Give the extent of all white blood cells.
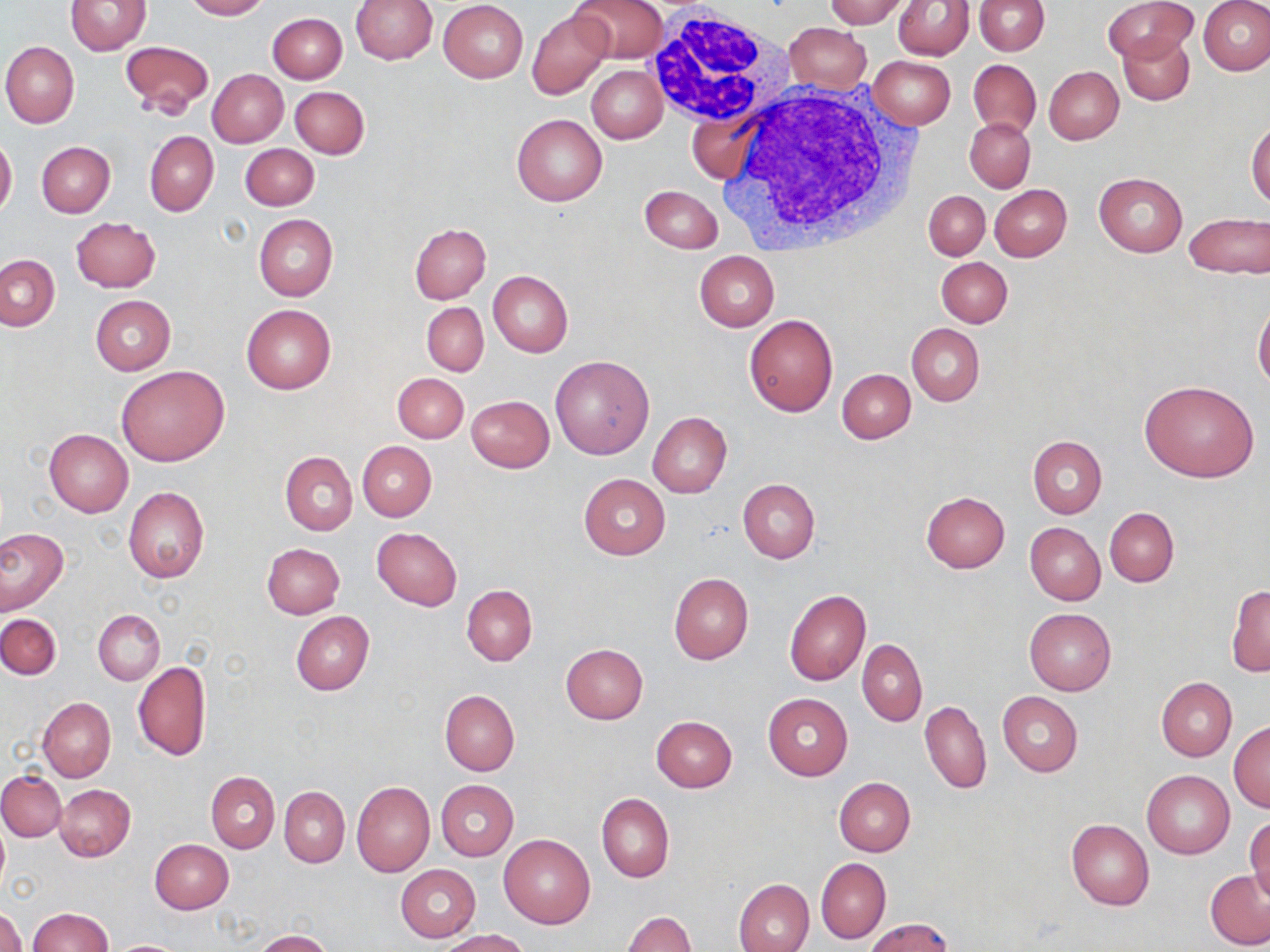

Approximate bounding boxes as named x1/y1/x2/y2 corners in pixels.
White blood cells: (x1=643, y1=9, x2=794, y2=129), (x1=716, y1=78, x2=918, y2=252).

Uninfected red blood cell locations: (x1=183, y1=0, x2=268, y2=20), (x1=350, y1=0, x2=438, y2=64), (x1=571, y1=0, x2=667, y2=63), (x1=824, y1=0, x2=909, y2=27), (x1=895, y1=0, x2=973, y2=59), (x1=1105, y1=0, x2=1193, y2=62), (x1=65, y1=1, x2=150, y2=56), (x1=439, y1=1, x2=528, y2=82), (x1=975, y1=1, x2=1049, y2=55), (x1=1198, y1=1, x2=1270, y2=76), (x1=527, y1=9, x2=613, y2=99), (x1=267, y1=12, x2=347, y2=83), (x1=784, y1=24, x2=871, y2=93), (x1=1118, y1=32, x2=1194, y2=106), (x1=120, y1=40, x2=214, y2=117), (x1=1, y1=41, x2=79, y2=127), (x1=868, y1=55, x2=956, y2=128), (x1=968, y1=59, x2=1040, y2=138), (x1=586, y1=65, x2=667, y2=143), (x1=1044, y1=66, x2=1123, y2=144), (x1=207, y1=69, x2=289, y2=146), (x1=291, y1=86, x2=369, y2=157), (x1=686, y1=105, x2=764, y2=186), (x1=511, y1=113, x2=607, y2=206), (x1=965, y1=117, x2=1035, y2=192), (x1=1247, y1=123, x2=1270, y2=208), (x1=145, y1=130, x2=219, y2=217), (x1=0, y1=136, x2=17, y2=216), (x1=36, y1=141, x2=115, y2=217), (x1=240, y1=143, x2=319, y2=211), (x1=1093, y1=173, x2=1187, y2=256), (x1=639, y1=184, x2=723, y2=252), (x1=990, y1=184, x2=1071, y2=260), (x1=924, y1=191, x2=989, y2=260), (x1=1184, y1=213, x2=1269, y2=280), (x1=254, y1=214, x2=338, y2=300), (x1=71, y1=216, x2=161, y2=292), (x1=409, y1=223, x2=491, y2=303), (x1=693, y1=251, x2=779, y2=331), (x1=1, y1=254, x2=59, y2=330), (x1=937, y1=256, x2=1012, y2=327), (x1=488, y1=270, x2=573, y2=356), (x1=90, y1=295, x2=175, y2=375), (x1=1254, y1=301, x2=1270, y2=392), (x1=422, y1=302, x2=488, y2=375), (x1=241, y1=304, x2=335, y2=394), (x1=744, y1=314, x2=837, y2=417), (x1=907, y1=324, x2=985, y2=406), (x1=549, y1=356, x2=654, y2=460), (x1=117, y1=365, x2=228, y2=467), (x1=838, y1=369, x2=916, y2=443), (x1=393, y1=373, x2=467, y2=442), (x1=1138, y1=380, x2=1260, y2=482), (x1=467, y1=396, x2=554, y2=472), (x1=647, y1=412, x2=732, y2=498), (x1=44, y1=429, x2=133, y2=517), (x1=1028, y1=435, x2=1107, y2=517), (x1=357, y1=441, x2=436, y2=521), (x1=281, y1=452, x2=357, y2=535), (x1=578, y1=474, x2=670, y2=559), (x1=738, y1=479, x2=820, y2=563), (x1=123, y1=487, x2=209, y2=583), (x1=920, y1=492, x2=1010, y2=573), (x1=1105, y1=507, x2=1179, y2=587), (x1=1025, y1=523, x2=1106, y2=605), (x1=372, y1=527, x2=462, y2=610), (x1=0, y1=529, x2=67, y2=614), (x1=262, y1=543, x2=345, y2=619), (x1=668, y1=573, x2=754, y2=664), (x1=1227, y1=584, x2=1270, y2=676), (x1=462, y1=585, x2=537, y2=666), (x1=784, y1=589, x2=869, y2=686), (x1=1024, y1=608, x2=1115, y2=695), (x1=93, y1=609, x2=164, y2=685), (x1=290, y1=613, x2=374, y2=695), (x1=0, y1=614, x2=61, y2=679), (x1=857, y1=638, x2=927, y2=726), (x1=560, y1=643, x2=648, y2=724), (x1=132, y1=660, x2=211, y2=761), (x1=1156, y1=677, x2=1236, y2=761), (x1=440, y1=690, x2=519, y2=775), (x1=997, y1=691, x2=1082, y2=777), (x1=763, y1=693, x2=853, y2=780), (x1=37, y1=698, x2=115, y2=782), (x1=920, y1=700, x2=991, y2=794), (x1=651, y1=716, x2=738, y2=792), (x1=1229, y1=721, x2=1269, y2=812), (x1=0, y1=770, x2=66, y2=841), (x1=1142, y1=770, x2=1234, y2=858), (x1=207, y1=772, x2=279, y2=853), (x1=834, y1=778, x2=915, y2=856), (x1=435, y1=780, x2=519, y2=861), (x1=352, y1=781, x2=434, y2=876), (x1=55, y1=784, x2=135, y2=861), (x1=279, y1=787, x2=349, y2=867), (x1=597, y1=793, x2=674, y2=882), (x1=1246, y1=813, x2=1269, y2=903), (x1=1066, y1=819, x2=1154, y2=910), (x1=0, y1=821, x2=9, y2=893), (x1=498, y1=834, x2=596, y2=928), (x1=150, y1=840, x2=234, y2=913), (x1=816, y1=858, x2=890, y2=943), (x1=396, y1=864, x2=481, y2=942), (x1=1205, y1=870, x2=1270, y2=950), (x1=733, y1=878, x2=813, y2=952), (x1=0, y1=908, x2=25, y2=952), (x1=28, y1=908, x2=112, y2=952), (x1=624, y1=911, x2=697, y2=952), (x1=866, y1=918, x2=954, y2=952), (x1=254, y1=930, x2=332, y2=952), (x1=438, y1=930, x2=530, y2=952), (x1=106, y1=939, x2=191, y2=951). Slide-level diagnosis: no evidence of blood parasites. One field of a larger specimen. Thin blood smear. Optical microscopy. May-Grünwald-Giemsa stain. Image is 1270×952 pixels. Captured at 1000x magnification.